Describe the morphology of the red blood cells.
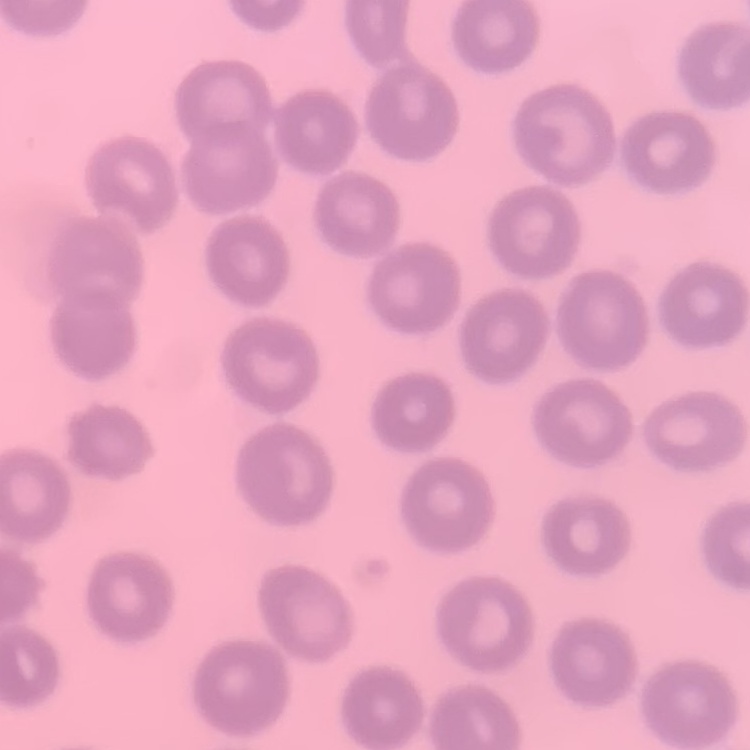
They show no rouleaux formation.

{
  "preparation": "thin blood film",
  "image_type": "square crop of a larger photomicrograph",
  "stain": "Field's or Giemsa"
}